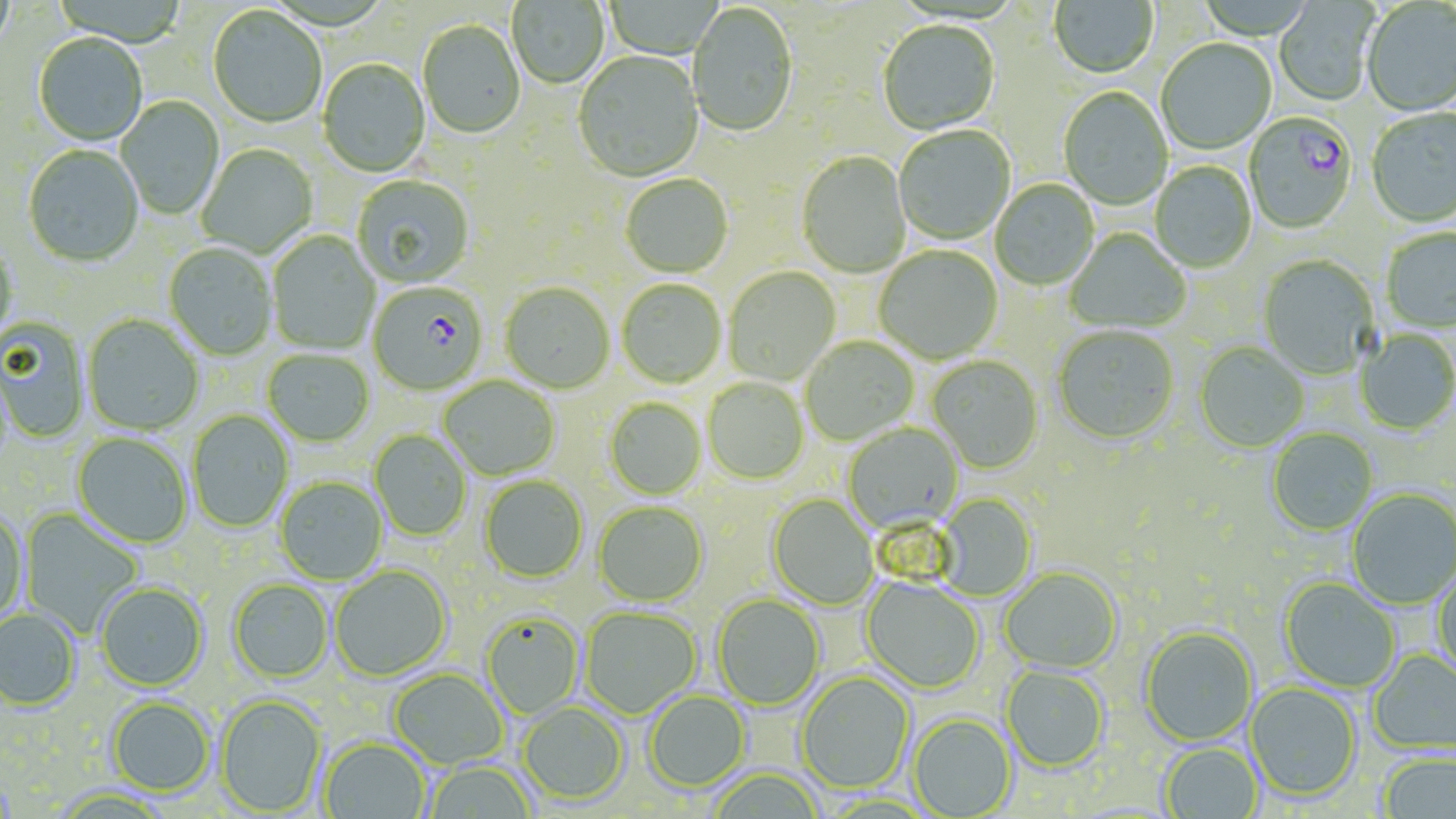

Approximate bounding boxes as [x1, y1, x2, y2] in pixels. Plasmodium falciparum-infected red blood cell locations: [1245, 113, 1358, 235], [368, 284, 488, 397]. Uninfected red blood cell locations: [0, 0, 15, 55], [507, 0, 610, 90], [1049, 0, 1159, 80], [1360, 1, 1456, 118], [1273, 2, 1378, 107], [687, 4, 797, 139], [207, 7, 327, 129], [417, 21, 525, 140], [878, 22, 1000, 137], [33, 35, 147, 148], [1156, 40, 1276, 156], [573, 53, 704, 184], [317, 59, 431, 179], [1058, 88, 1173, 210], [116, 96, 225, 220], [1366, 109, 1456, 229], [894, 126, 1016, 246], [196, 145, 318, 260], [23, 146, 144, 269], [796, 153, 912, 279], [1150, 162, 1257, 273], [620, 175, 734, 279], [352, 176, 474, 289], [990, 180, 1100, 291], [1380, 228, 1456, 333], [1065, 229, 1191, 335], [267, 231, 381, 355], [0, 239, 19, 350], [163, 244, 277, 361], [874, 246, 1003, 365], [1258, 255, 1381, 381], [724, 267, 841, 387], [617, 280, 726, 389], [500, 283, 615, 394], [83, 315, 203, 436], [0, 318, 90, 443], [1053, 327, 1179, 446], [1354, 329, 1456, 437], [801, 336, 919, 446], [1194, 343, 1308, 453], [263, 350, 374, 447], [927, 356, 1043, 474], [439, 376, 561, 481], [703, 377, 809, 485], [605, 398, 707, 500], [187, 410, 294, 534], [843, 424, 964, 533], [1267, 428, 1378, 536], [369, 429, 472, 541], [72, 432, 193, 549], [479, 475, 588, 584], [275, 476, 388, 585], [1347, 489, 1456, 610], [937, 494, 1037, 601], [767, 495, 878, 610], [593, 502, 707, 606], [19, 509, 144, 637], [0, 510, 28, 628], [1431, 564, 1456, 683], [329, 565, 452, 682], [999, 568, 1122, 675], [860, 577, 984, 695], [1279, 578, 1400, 693], [228, 580, 333, 683], [95, 583, 209, 692], [712, 594, 825, 711], [580, 607, 702, 719], [0, 610, 81, 711], [480, 610, 584, 719], [1140, 626, 1258, 747], [1369, 648, 1456, 756], [1000, 666, 1109, 772], [388, 669, 507, 769], [796, 672, 915, 795], [1246, 683, 1361, 803], [643, 691, 751, 792], [216, 694, 327, 816], [107, 697, 215, 797], [517, 702, 628, 806], [908, 714, 1017, 818], [319, 737, 430, 819], [1158, 743, 1263, 818], [1378, 753, 1456, 818], [423, 761, 536, 819], [706, 768, 826, 819]. Slide-level diagnosis: Plasmodium falciparum. Optical microscopy. Thin blood film. Captured at 1000x magnification. May-Grünwald-Giemsa stain. Single field of view. Image is 1456×819 pixels.